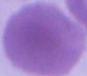

Summary:
  - Modality: photomicrograph
  - Identification: erythrocyte
  - Magnification: 1000x